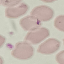 Malaria status: uninfected. Cell patch, automatically extracted from a larger field of view and resized to 64 × 64 pixels. Photographed with a smartphone camera at the microscope eyepiece. Giemsa stain. Thin blood film.